Report the malaria status of this cell.
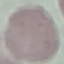

It is uninfected.

Summary:
  - Stain: Giemsa
  - Preparation: thin blood smear
  - Capture: smartphone through the microscope eyepiece
  - Image type: cell patch, automatically extracted from a larger field of view and resized to 64 × 64 pixels